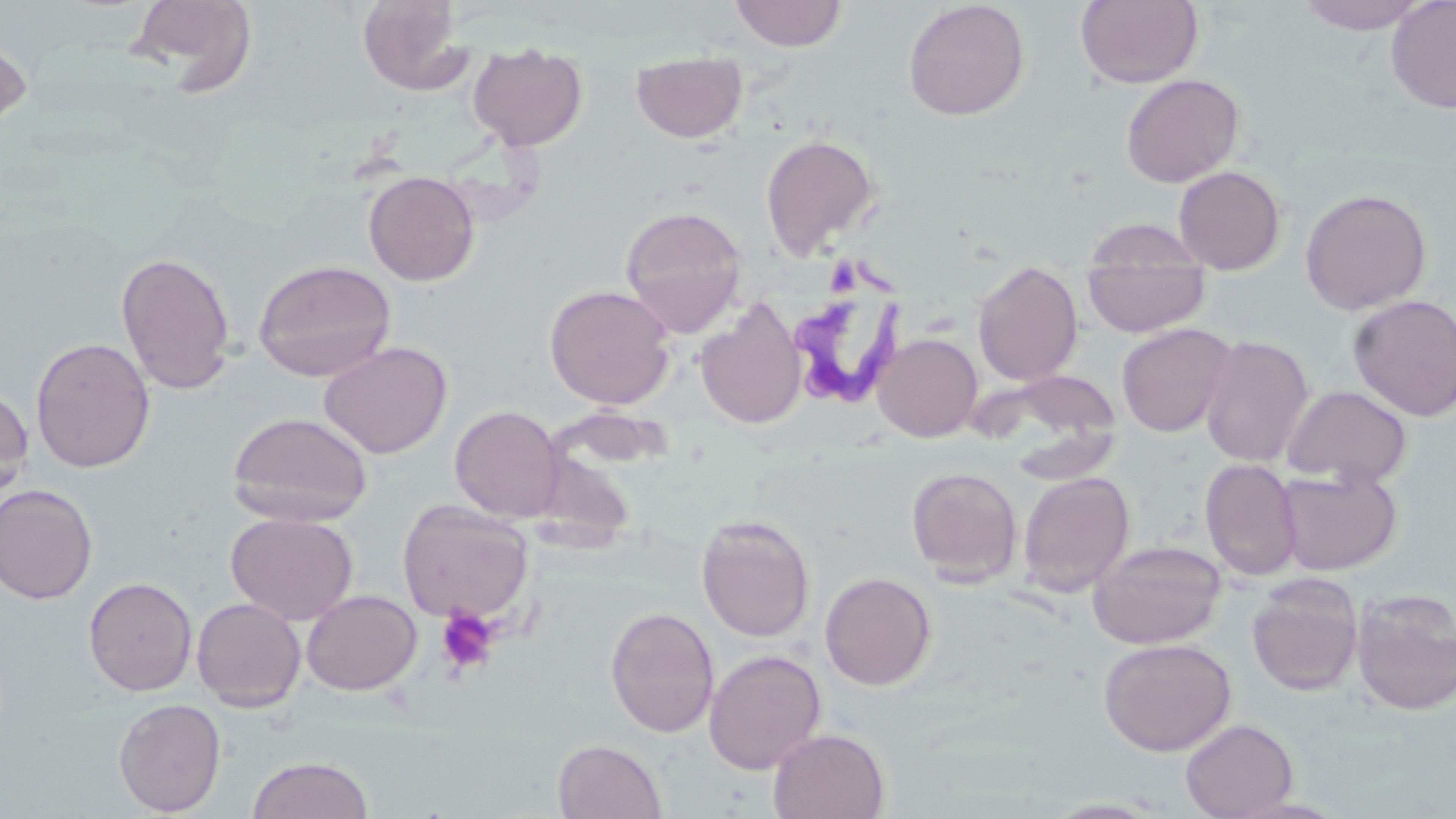
{
  "slide_level_diagnosis": "Trypanosoma brucei",
  "uninfected_red_blood_cell_locations": "approximate bounding boxes as (x1, y1, x2, y2) in pixels: (126, 0, 258, 93), (729, 0, 849, 51), (903, 0, 1030, 121), (1075, 0, 1204, 88), (1295, 0, 1432, 35), (1386, 0, 1456, 114), (356, 1, 476, 96), (0, 33, 33, 134), (468, 42, 588, 151), (631, 50, 747, 143), (1121, 73, 1245, 188), (760, 134, 882, 261), (1173, 165, 1286, 275), (363, 170, 480, 287), (1299, 187, 1432, 316), (619, 205, 748, 338), (1082, 237, 1211, 338), (116, 252, 237, 394), (253, 259, 397, 382), (972, 260, 1083, 387), (544, 284, 676, 409), (1347, 295, 1456, 422), (694, 298, 807, 430), (1116, 322, 1237, 438), (872, 332, 982, 443), (1199, 335, 1314, 468), (30, 336, 156, 473), (317, 341, 453, 460), (989, 368, 1126, 474), (0, 385, 34, 507), (1281, 385, 1412, 488), (450, 405, 565, 522), (227, 411, 373, 526), (1201, 458, 1302, 581), (1276, 465, 1402, 576), (906, 466, 1023, 586), (1017, 471, 1135, 596), (0, 483, 98, 603), (397, 499, 533, 625), (225, 511, 358, 625), (696, 514, 816, 642), (1088, 539, 1227, 649), (820, 571, 937, 690), (1247, 574, 1364, 696), (83, 576, 197, 696), (301, 589, 422, 696), (1351, 589, 1456, 716), (191, 597, 306, 712), (605, 605, 720, 738), (1098, 637, 1237, 757), (704, 649, 827, 774), (113, 697, 227, 816), (1180, 717, 1299, 819), (769, 728, 890, 818), (553, 740, 667, 819), (245, 755, 375, 819)",
  "trypanosoma_brucei_locations": "approximate bounding boxes as (x1, y1, x2, y2) in pixels: (792, 208, 920, 408)",
  "modality": "light microscopy",
  "field_of_view": "one of a larger specimen",
  "preparation": "thin blood smear",
  "platelet_locations": "approximate bounding boxes as (x1, y1, x2, y2) in pixels: (435, 607, 500, 676)",
  "image_size": "1456×819 pixels",
  "stain": "May-Grünwald-Giemsa",
  "magnification": "1000x"
}